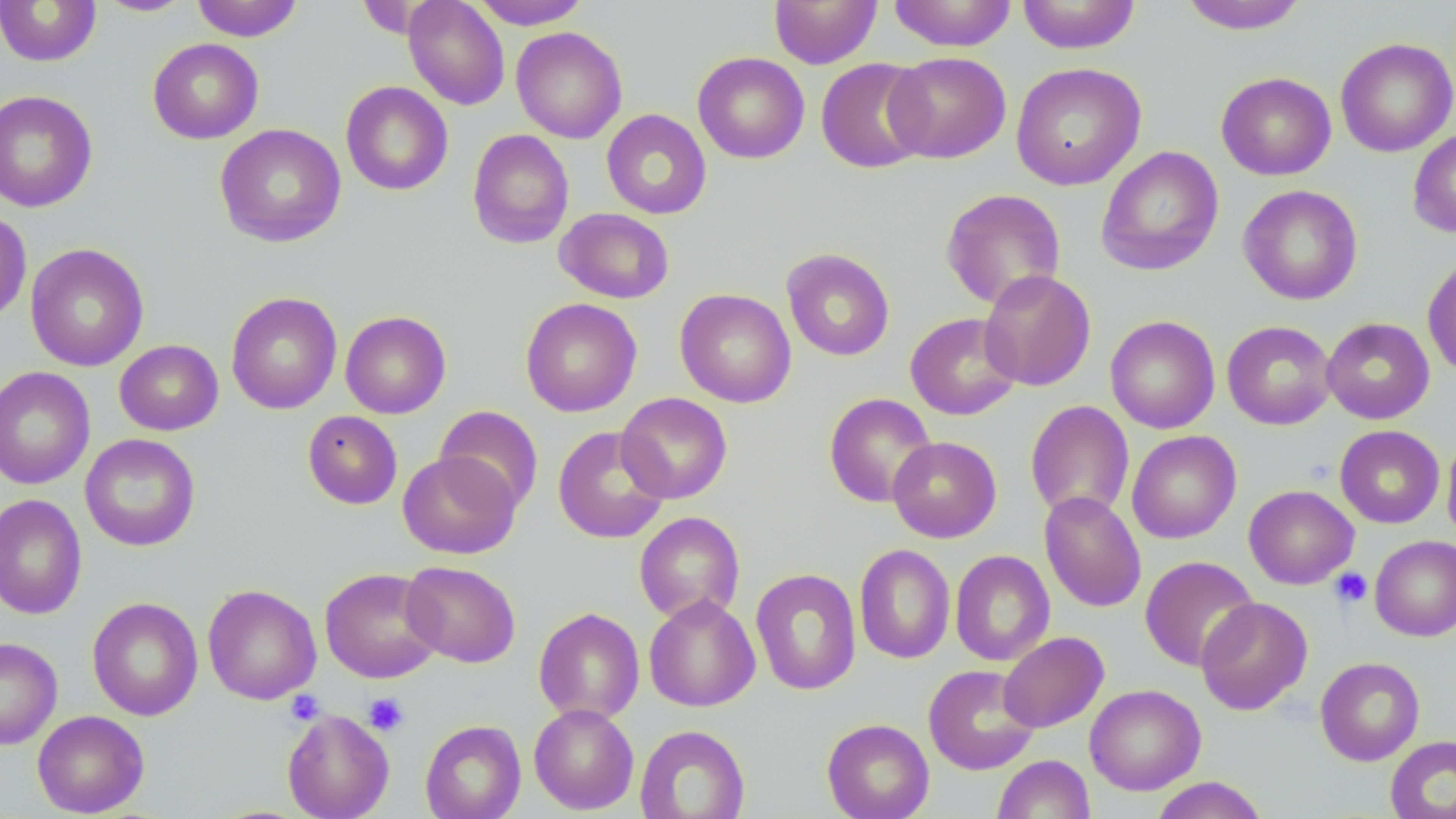

slide-level diagnosis = no evidence of blood parasites
preparation = thin blood smear
image size = 1456×819 pixels
platelet locations = approximate bounding boxes as (x1, y1, x2, y2) in pixels: (1329, 567, 1372, 609), (285, 690, 324, 725), (363, 692, 409, 736)
uninfected red blood cell locations = approximate bounding boxes as (x1, y1, x2, y2) in pixels: (0, 0, 101, 66), (191, 0, 304, 41), (403, 0, 510, 110), (470, 0, 591, 29), (769, 0, 881, 68), (887, 0, 1017, 52), (1016, 0, 1141, 54), (94, 1, 195, 17), (1179, 1, 1308, 34), (511, 26, 627, 143), (1335, 37, 1456, 158), (148, 38, 264, 144), (884, 51, 1011, 163), (693, 52, 809, 163), (815, 57, 932, 174), (1010, 62, 1146, 190), (1216, 71, 1337, 180), (341, 81, 453, 196), (0, 90, 99, 213), (601, 109, 712, 219), (215, 124, 346, 248), (467, 129, 574, 249), (1408, 129, 1456, 239), (1096, 146, 1224, 276), (1238, 185, 1363, 305), (941, 188, 1066, 310), (555, 208, 674, 303), (0, 209, 32, 326), (25, 243, 149, 371), (781, 248, 895, 361), (1422, 252, 1456, 379), (979, 269, 1096, 391), (675, 288, 796, 407), (226, 292, 342, 414), (520, 298, 641, 417), (340, 311, 451, 418), (905, 312, 1022, 420), (1105, 316, 1220, 434), (1321, 317, 1435, 424), (1222, 321, 1336, 430), (114, 339, 223, 435), (0, 366, 95, 490), (617, 392, 732, 504), (824, 393, 937, 508), (1025, 400, 1135, 521), (435, 405, 543, 513), (303, 410, 403, 509), (553, 425, 671, 544), (1335, 425, 1445, 528), (1127, 430, 1241, 544), (80, 433, 201, 551), (1442, 433, 1456, 545), (887, 436, 1001, 542), (397, 451, 521, 559), (1244, 484, 1359, 589), (1039, 490, 1146, 613), (0, 493, 87, 620), (634, 511, 745, 624), (1370, 535, 1456, 641), (854, 544, 955, 664), (950, 550, 1055, 666), (1140, 555, 1259, 672), (401, 561, 520, 668), (319, 567, 443, 683), (750, 568, 862, 695), (202, 584, 321, 705), (644, 594, 760, 712), (87, 596, 203, 721), (1195, 596, 1313, 715), (533, 607, 645, 724), (998, 632, 1109, 733), (0, 637, 62, 749), (1315, 656, 1425, 766), (923, 664, 1040, 775), (1085, 684, 1206, 795), (528, 703, 639, 814), (281, 708, 394, 819), (32, 710, 149, 817), (822, 718, 934, 819), (420, 720, 526, 819), (635, 725, 750, 818), (1385, 735, 1456, 819), (992, 754, 1095, 818), (1149, 777, 1269, 819)
magnification = 1000x
modality = optical microscopy
field of view = one of a larger specimen
stain = May-Grünwald-Giemsa